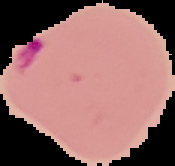
Summary:
  - Preparation: thin blood smear
  - Result: malaria parasites identified
  - Image type: segmented cell region with the area outside set to black
  - Image size: 175×166 pixels